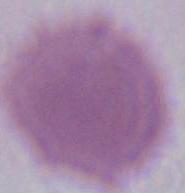 Photomicrograph. Captured at 1000x magnification. An erythrocyte is shown.